Report the malaria status of this cell.
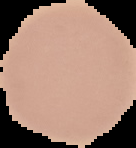
It is uninfected.

Summary:
  - Preparation: thin blood film
  - Image type: cell region segmented out of the field of view; surrounding area masked to black
  - Image size: 136×148 pixels